Classify this cell by malaria status.
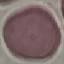

It is uninfected.

preparation = thin blood smear
stain = Giemsa
image type = automatically extracted cell patch, resized to 64 × 64 pixels
capture = smartphone through the microscope eyepiece